Assess the morphology of the erythrocytes.
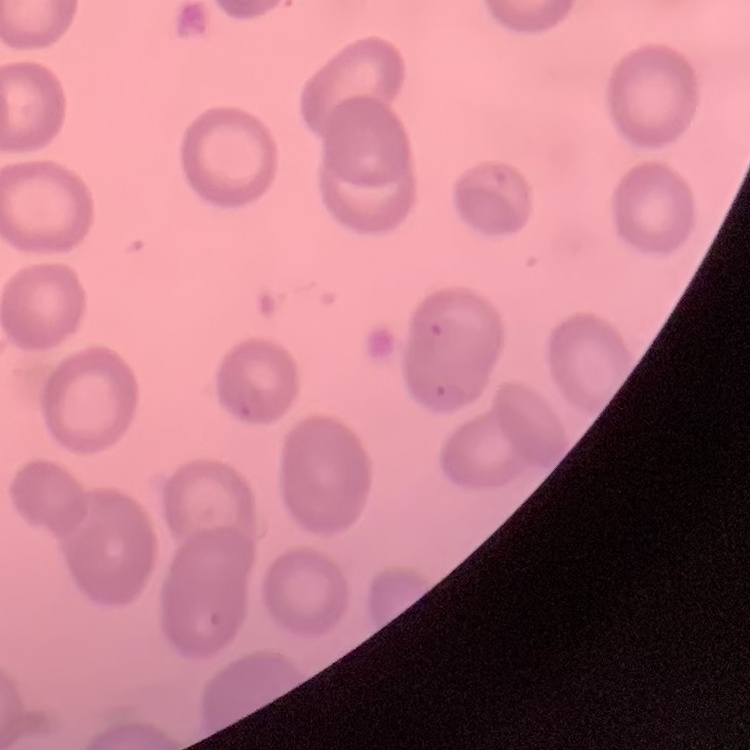

They show no rouleaux formation.

image type = square crop of a larger photomicrograph
stain = Field's or Giemsa
preparation = thin peripheral smear